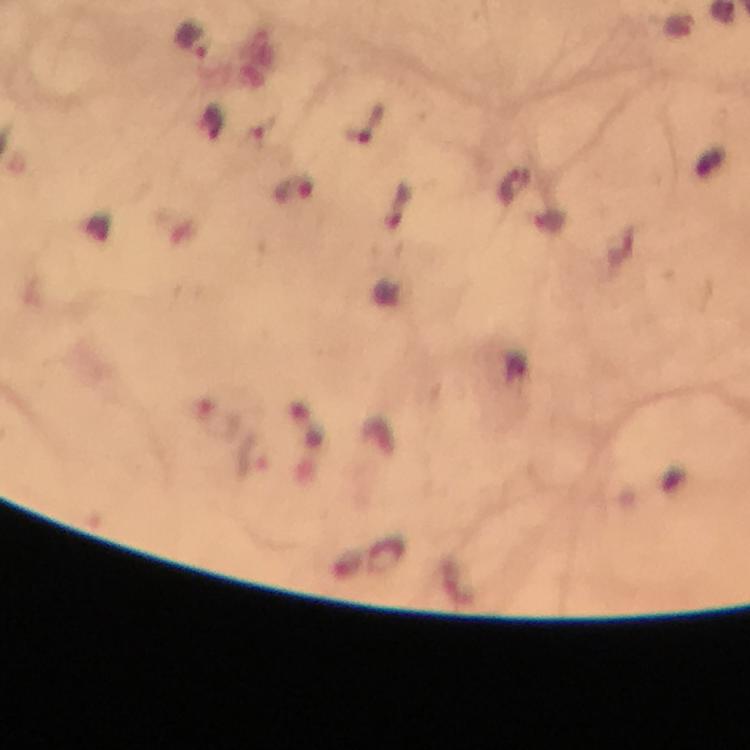
capture = smartphone photograph through a microscope
preparation = thick blood film
stain = Giemsa
immersion oil = applied
image size = 750×750 pixels
cropped from = one field of view
context = from a malaria diagnostic workup
malaria parasite locations = approximate centers as [x, y] in pixels: [192, 40], [366, 125], [293, 187]
magnification = 100x